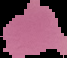
Summary:
  - Image size: 67×58 pixels
  - Result: no malaria parasites detected
  - Preparation: thin blood smear
  - Image type: cell region segmented out of the field of view; surrounding area masked to black